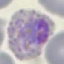

Summary:
  - Malaria status: parasitized
  - Capture: smartphone through the microscope eyepiece
  - Preparation: thin smear
  - Stain: Giemsa
  - Image type: automatically extracted cell patch, resized to 64 × 64 pixels